Classify this cell by malaria status.
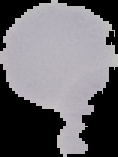

It is uninfected.

{
  "image_type": "segmented cell region on a black background",
  "preparation": "thin blood film",
  "image_size": "118×157 pixels"
}